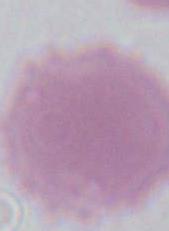

A red blood cell is shown. Captured at 1000x magnification. Photomicrograph.